Outline each blood parasite and name the species.
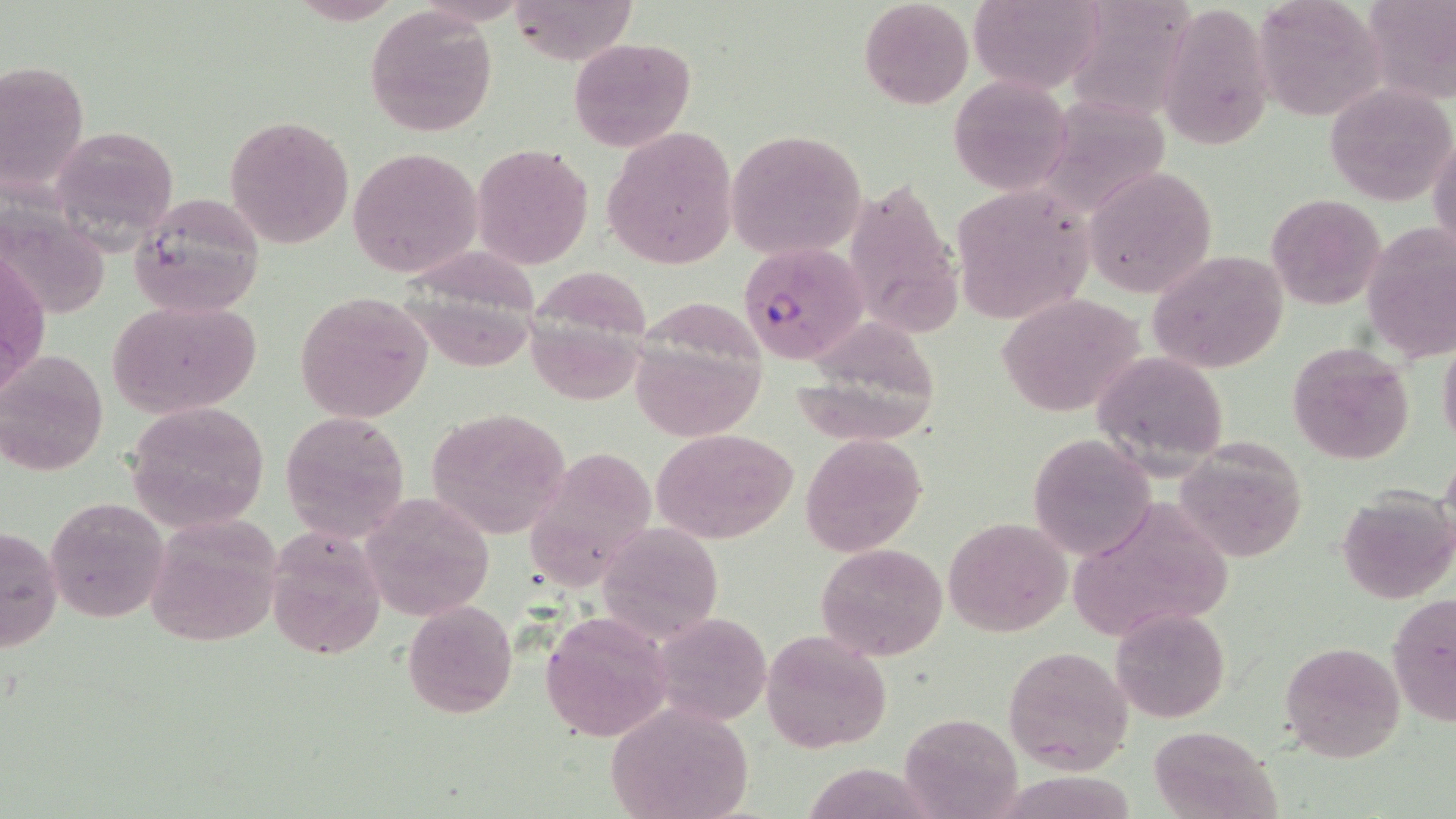

Approximate bounding boxes as named x1/y1/x2/y2 corners in pixels.
Plasmodium falciparum-infected red blood cells: (x1=738, y1=240, x2=868, y2=365).
No Plasmodium ovale, Plasmodium malariae, Plasmodium vivax, Babesia divergens, or Trypanosoma brucei observed.

slide-level diagnosis = Plasmodium falciparum
stain = May-Grünwald-Giemsa
image size = 1456×819 pixels
modality = optical microscopy
field of view = single
uninfected red blood cell locations = approximate bounding boxes as named x1/y1/x2/y2 corners in pixels: (x1=286, y1=0, x2=407, y2=25), (x1=507, y1=0, x2=634, y2=66), (x1=857, y1=0, x2=976, y2=111), (x1=969, y1=0, x2=1106, y2=97), (x1=1254, y1=0, x2=1386, y2=121), (x1=1364, y1=0, x2=1456, y2=104), (x1=1086, y1=2, x2=1212, y2=125), (x1=1160, y1=2, x2=1274, y2=151), (x1=363, y1=6, x2=499, y2=137), (x1=568, y1=36, x2=694, y2=154), (x1=0, y1=60, x2=89, y2=198), (x1=947, y1=76, x2=1072, y2=195), (x1=1327, y1=83, x2=1455, y2=205), (x1=1047, y1=87, x2=1169, y2=216), (x1=224, y1=115, x2=353, y2=250), (x1=50, y1=123, x2=180, y2=246), (x1=602, y1=127, x2=738, y2=270), (x1=1430, y1=128, x2=1455, y2=256), (x1=725, y1=130, x2=865, y2=261), (x1=472, y1=144, x2=593, y2=269), (x1=348, y1=146, x2=481, y2=280), (x1=1082, y1=166, x2=1218, y2=300), (x1=845, y1=174, x2=962, y2=341), (x1=951, y1=186, x2=1097, y2=325), (x1=128, y1=193, x2=267, y2=316), (x1=1265, y1=194, x2=1385, y2=311), (x1=1361, y1=223, x2=1455, y2=366), (x1=413, y1=246, x2=547, y2=371), (x1=1147, y1=248, x2=1288, y2=376), (x1=1, y1=250, x2=49, y2=396), (x1=538, y1=268, x2=654, y2=405), (x1=638, y1=292, x2=768, y2=444), (x1=295, y1=293, x2=434, y2=422), (x1=996, y1=294, x2=1145, y2=418), (x1=105, y1=299, x2=262, y2=418), (x1=798, y1=318, x2=942, y2=450), (x1=1438, y1=335, x2=1456, y2=452), (x1=1285, y1=339, x2=1419, y2=467), (x1=0, y1=349, x2=108, y2=477), (x1=1090, y1=350, x2=1231, y2=476), (x1=124, y1=402, x2=270, y2=531), (x1=425, y1=407, x2=571, y2=537), (x1=280, y1=409, x2=411, y2=544), (x1=652, y1=428, x2=797, y2=543), (x1=800, y1=435, x2=924, y2=554), (x1=1028, y1=435, x2=1156, y2=559), (x1=1176, y1=439, x2=1309, y2=560), (x1=522, y1=446, x2=658, y2=596), (x1=1336, y1=488, x2=1455, y2=605), (x1=360, y1=493, x2=496, y2=623), (x1=44, y1=496, x2=168, y2=624), (x1=1060, y1=500, x2=1237, y2=637), (x1=141, y1=515, x2=282, y2=649), (x1=942, y1=517, x2=1072, y2=637), (x1=1, y1=523, x2=63, y2=652), (x1=600, y1=525, x2=725, y2=638), (x1=265, y1=527, x2=385, y2=661), (x1=817, y1=542, x2=948, y2=662), (x1=1387, y1=593, x2=1455, y2=728), (x1=402, y1=600, x2=517, y2=719), (x1=1111, y1=607, x2=1232, y2=723), (x1=650, y1=611, x2=772, y2=727), (x1=539, y1=614, x2=672, y2=742), (x1=760, y1=630, x2=892, y2=752), (x1=1279, y1=640, x2=1405, y2=764), (x1=1002, y1=646, x2=1134, y2=773), (x1=606, y1=701, x2=756, y2=819), (x1=899, y1=712, x2=1022, y2=819), (x1=1146, y1=725, x2=1279, y2=818)
magnification = 1000x
preparation = thin blood smear